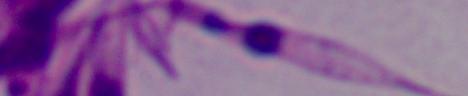

{
  "identification": "Leishmania",
  "modality": "photomicrograph",
  "magnification": "1000x"
}